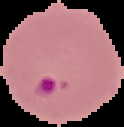

image_type: cell region segmented out of the field of view; surrounding area masked to black
preparation: thin blood film
result: malaria parasites detected
image_size: 124×127 pixels